Name the blood parasite species.
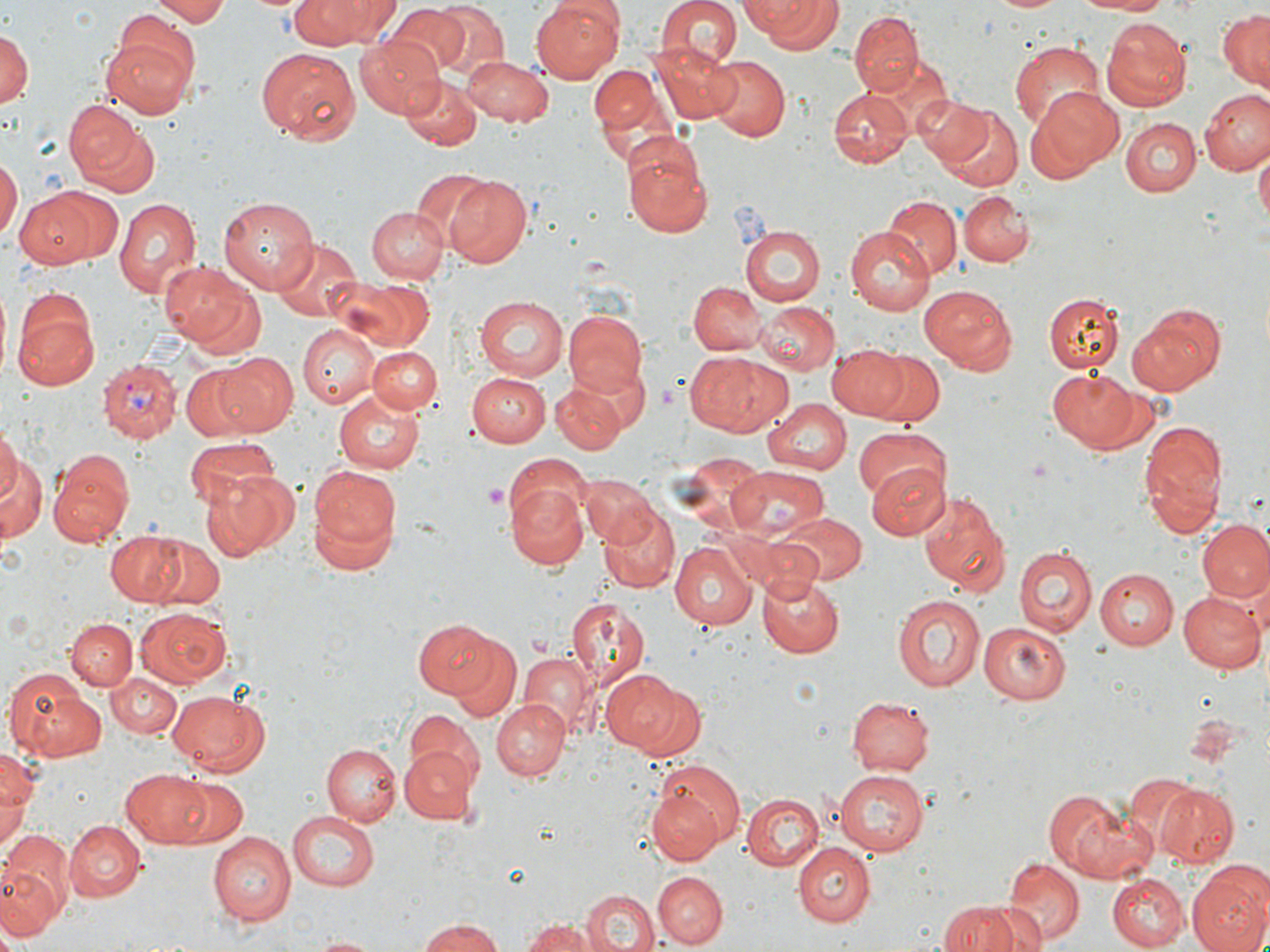
Plasmodium vivax.

image_size: 1270×952 pixels
modality: light microscopy
magnification: 1000x
uninfected_red_blood_cell_locations: 'approximate bounding boxes as (x1,y1)-(x2,y2) corner pairs in pixels: (142,0)-(231,24), (290,0)-(389,45), (654,0)-(741,73), (742,0)-(842,53), (994,0)-(1065,14), (1072,0)-(1174,15), (425,1)-(511,81), (531,1)-(624,84), (383,6)-(471,77), (849,9)-(923,96), (1216,10)-(1270,92), (1102,20)-(1193,109), (0,29)-(34,110), (101,30)-(198,116), (354,37)-(445,118), (1009,40)-(1106,136), (652,41)-(743,124), (255,49)-(361,144), (461,55)-(552,125), (703,55)-(790,142), (863,59)-(951,139), (588,60)-(679,167), (398,76)-(482,150), (1028,86)-(1121,178), (829,87)-(910,168), (1200,90)-(1270,175), (915,95)-(1000,173), (65,102)-(161,200), (940,105)-(1025,191), (1120,117)-(1201,198), (622,136)-(714,238), (1254,147)-(1269,222), (0,158)-(20,246), (413,167)-(494,252), (442,172)-(532,267), (16,188)-(119,269), (958,191)-(1035,267), (220,196)-(322,292), (885,196)-(962,278), (113,198)-(202,301), (366,206)-(447,284), (741,226)-(824,304), (845,228)-(934,315), (269,237)-(360,324), (162,261)-(260,352), (331,276)-(435,354), (686,280)-(766,355), (918,283)-(1016,374), (1044,293)-(1123,372), (475,295)-(567,380), (12,299)-(99,392), (1126,300)-(1226,397), (758,302)-(840,377), (562,309)-(648,398), (298,325)-(379,408), (553,331)-(643,449), (366,344)-(442,417), (826,345)-(906,420), (863,348)-(944,427), (215,351)-(300,435), (687,352)-(787,438), (180,364)-(263,440), (1046,367)-(1145,450), (466,373)-(551,447), (553,383)-(626,453), (335,391)-(425,473), (763,396)-(851,474), (1137,420)-(1228,537), (0,423)-(22,513), (851,426)-(951,503), (184,437)-(278,509), (0,443)-(46,548), (48,453)-(134,549), (501,453)-(592,529), (681,453)-(772,538), (307,461)-(402,567), (867,462)-(951,540), (726,465)-(830,544), (197,470)-(297,562), (581,474)-(654,547), (504,481)-(590,570), (918,490)-(1011,598), (597,501)-(680,595), (772,513)-(866,587), (1198,519)-(1270,605), (104,532)-(197,607), (144,537)-(226,609), (670,542)-(756,630), (1012,544)-(1098,637), (1093,568)-(1178,649), (757,571)-(843,657), (1177,589)-(1266,676), (893,592)-(985,692), (564,598)-(649,683), (136,608)-(230,688), (65,619)-(136,690), (413,620)-(497,697), (977,620)-(1073,705), (445,636)-(521,721), (519,654)-(596,733), (5,668)-(106,763), (602,670)-(704,758), (107,672)-(183,737), (166,688)-(271,775), (846,695)-(935,776), (490,697)-(571,781), (405,710)-(484,796), (322,744)-(400,826), (399,745)-(479,823), (0,748)-(36,856), (120,767)-(214,849), (834,768)-(930,854), (1123,773)-(1213,860), (646,777)-(737,865), (173,779)-(250,848), (1156,784)-(1238,867), (1041,790)-(1152,882), (742,793)-(826,869), (287,811)-(378,891), (65,819)-(146,900), (1,830)-(74,932), (208,833)-(294,925), (791,841)-(875,925), (1002,856)-(1082,946), (0,866)-(57,946), (1186,866)-(1270,952), (653,871)-(728,948), (1109,874)-(1187,950), (581,889)-(657,952), (936,899)-(1023,952), (976,902)-(1050,952), (416,918)-(507,952), (519,918)-(606,952), (306,936)-(385,952)'
stain: May-Grünwald-Giemsa
platelet_locations: 'approximate bounding boxes as (x1,y1)-(x2,y2) corner pairs in pixels: (483,481)-(509,510)'
plasmodium_vivax_infected_red_blood_cell_locations: 'approximate bounding boxes as (x1,y1)-(x2,y2) corner pairs in pixels: (101,358)-(181,444)'
field_of_view: one of a larger specimen
preparation: thin blood smear